Comment on the morphology of the erythrocytes.
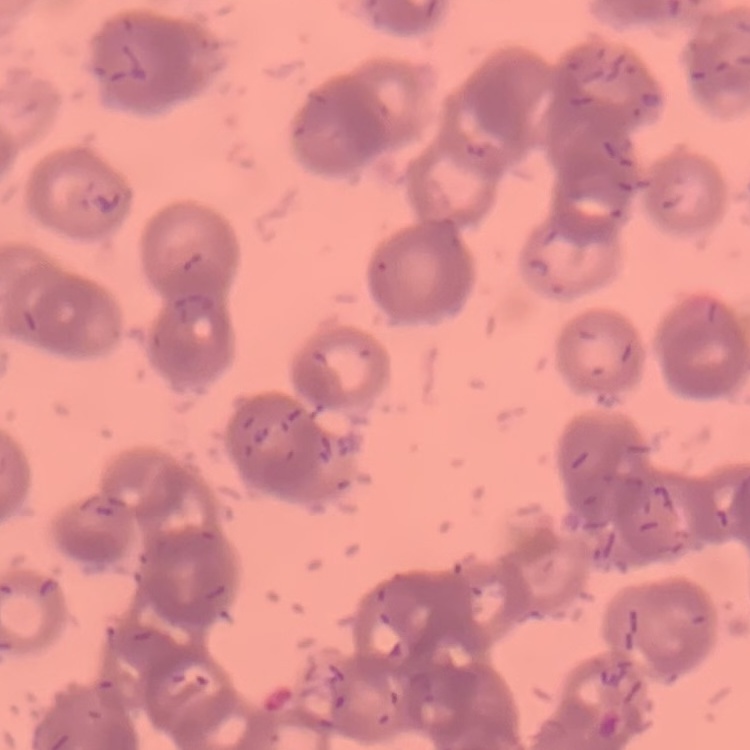

Rouleaux formation.

image type = one tile cut from a larger photomicrograph
preparation = thin peripheral smear
stain = Field's or Giemsa